Assess this cell for malaria.
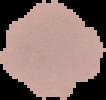
It is parasitized.

preparation = thin blood smear
image type = segmented cell region with the area outside set to black
image size = 106×100 pixels